Name the parasite shown.
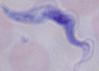

This is a trypanosome.

Summary:
  - Magnification: 1000x
  - Modality: photomicrograph